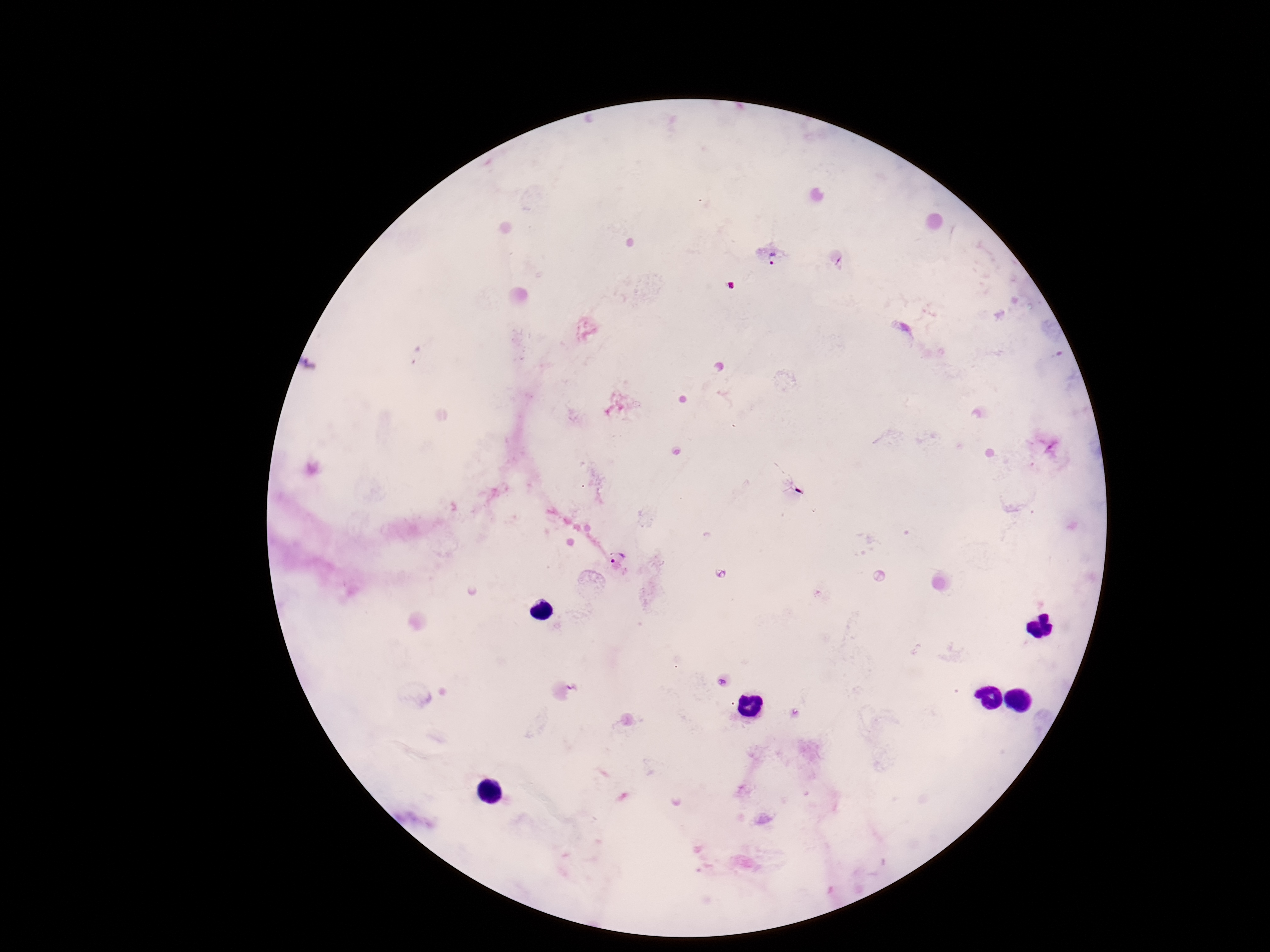
Approximate centers as [x, y] in pixels.
Summary:
  - Plasmodium parasite locations: [773, 256], [616, 557]
  - Capture: smartphone camera through the microscope eyepiece
  - Field of view: single
  - Magnification: 100x
  - Preparation: thick peripheral-blood smear
  - Patient malaria status: positive
  - Stain: Giemsa
  - Image size: 1270×952 pixels